Report the malaria status of this cell.
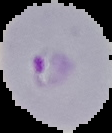

Parasitized.

Image is 112×133 pixels. Segmented cell region on a black background. From a thin blood smear.